Locate leukocytes (white blood cells).
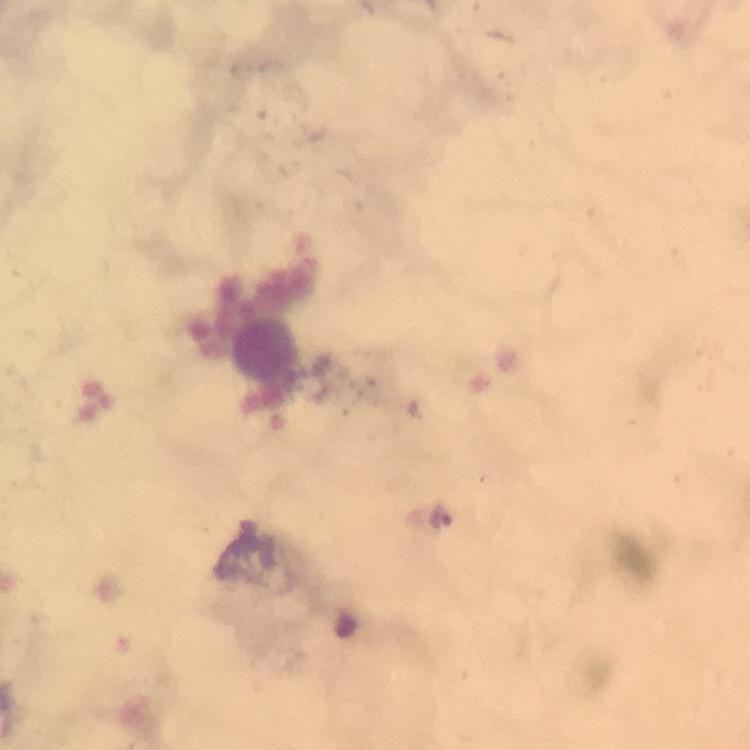

Approximate centers as (x, y) in pixels.
Leukocytes: (267, 346).

Plasmodium parasite locations: (441, 518). Cropped region of a single field of view. Immersion oil was used. Thick blood film. Photographed with a smartphone mounted on the microscope. At 100x magnification. From a diagnostic examination for malaria. Image is 750×750 pixels. Giemsa-stained preparation.